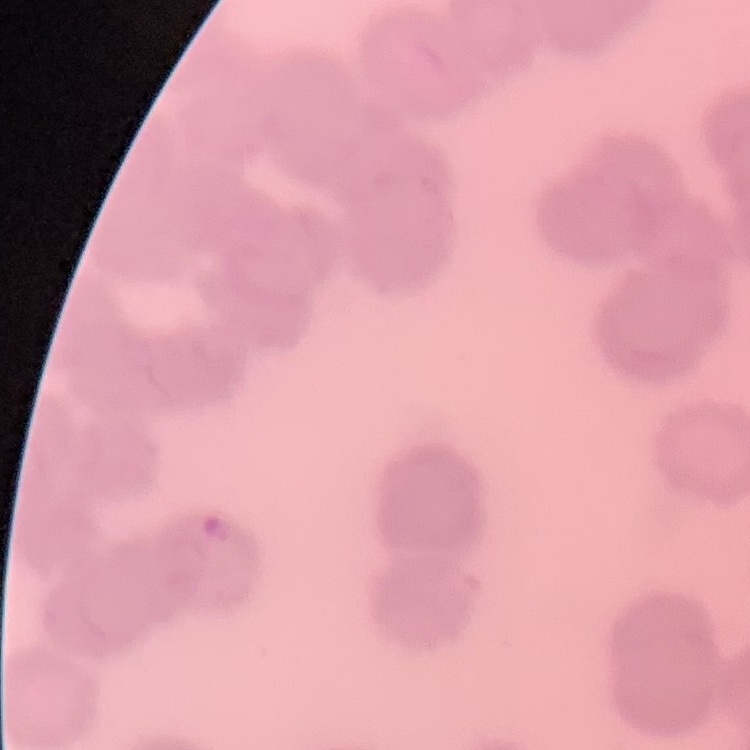

Summary:
  - Erythrocyte morphology: rouleaux formation
  - Preparation: thin peripheral smear
  - Stain: Field's or Giemsa
  - Image type: one tile cut from a larger photomicrograph